Assess this cell for malaria.
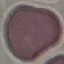
It is uninfected.

Summary:
  - Capture: smartphone through the microscope eyepiece
  - Stain: Giemsa
  - Preparation: thin blood smear
  - Image type: automatically extracted cell patch, resized to 64 × 64 pixels